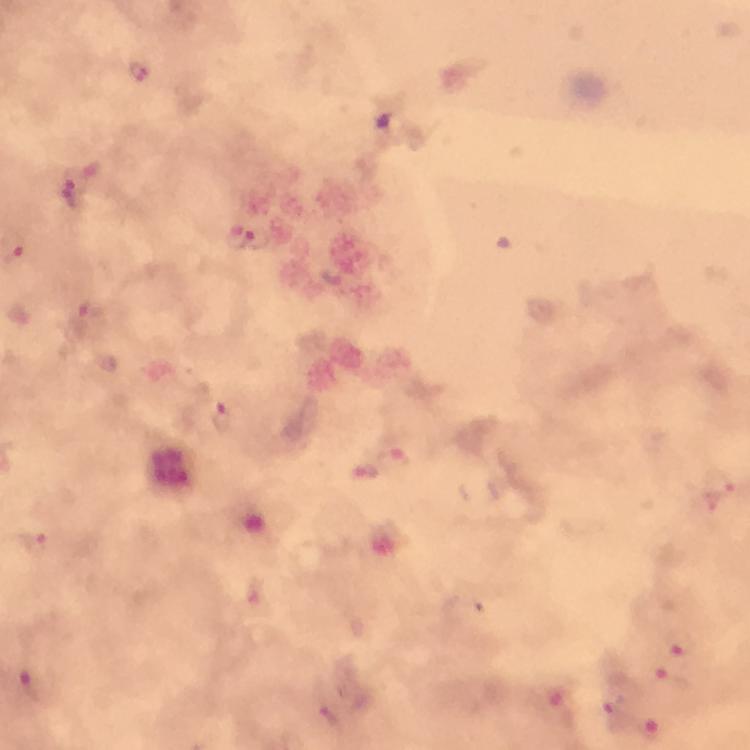
capture = smartphone camera through the microscope
stain = Giemsa
context = from a malaria diagnostic workup
immersion oil = applied
Plasmodium parasite locations = approximate centers as (x, y) in pixels: (137, 73), (73, 181), (71, 199), (256, 241), (91, 312), (221, 416), (393, 462), (719, 489), (34, 543), (683, 647), (674, 681), (35, 686), (612, 714), (330, 718), (651, 727)
image size = 750×750 pixels
magnification = 100x
cropped from = one field of view
preparation = thick smear